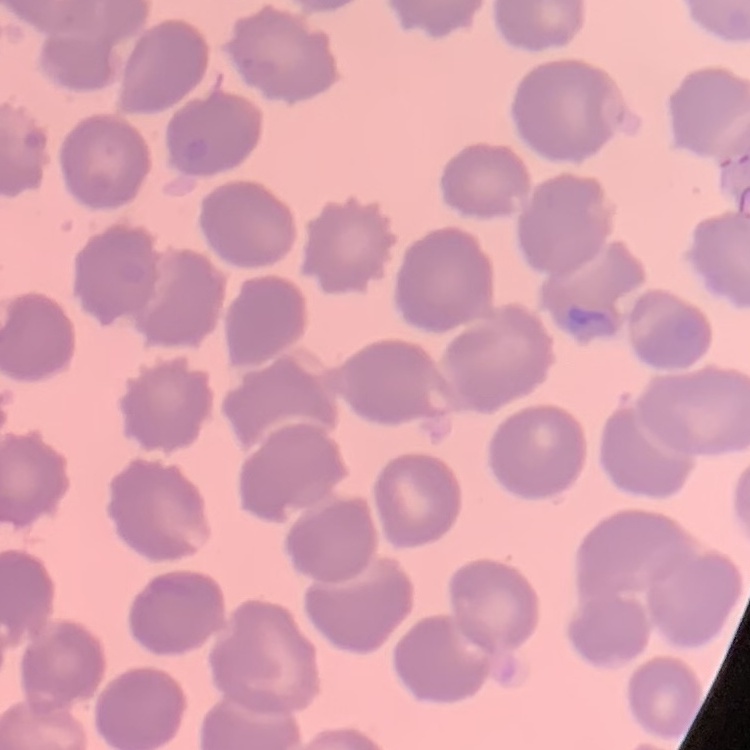

red blood cell morphology = no rouleaux formation
preparation = thin peripheral smear
image type = square crop of a larger photomicrograph
stain = Field's or Giemsa